Report the malaria status of this cell.
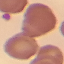
It is uninfected.

Thin blood smear. Automatically extracted cell patch, resized to 64 × 64 pixels. Giemsa stain. Acquired by smartphone through the microscope eyepiece.